Classify this cell by malaria status.
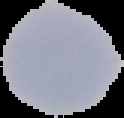
Uninfected.

Cell region segmented out of the field of view; the surrounding area is masked to black. From a thin blood smear. Image is 124×118 pixels.